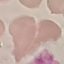
Result: no malaria parasites seen. Cell patch, automatically extracted from a larger field of view and resized to 64 × 64 pixels. Giemsa stain. Acquired by smartphone through the microscope eyepiece. Thin smear of blood.